State which parasite is depicted.
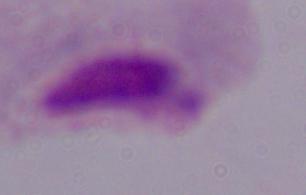

A trichomonad.

Micrograph. 1000x magnification.